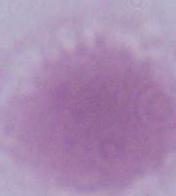
A red blood cell is shown. Photomicrograph. 1000x magnification.